Identify the blood parasite species.
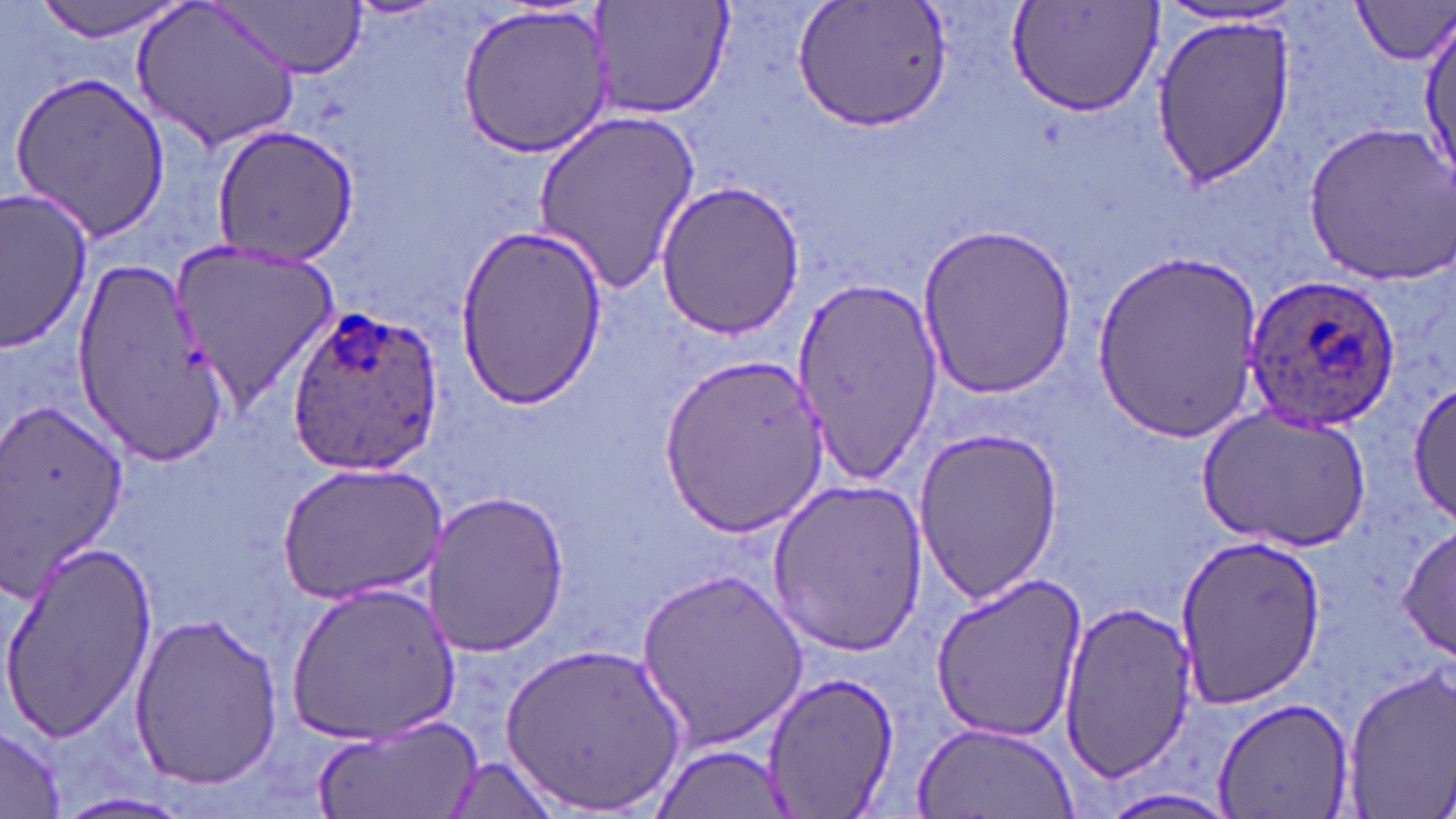

Plasmodium ovale.

Summary:
  - Coordinate format: approximate bounding boxes as [x1, y1, x2, y2] in pixels
  - Uninfected red blood cell locations: [31, 0, 192, 43], [131, 0, 305, 153], [597, 0, 735, 122], [792, 0, 953, 130], [1008, 0, 1165, 120], [1353, 2, 1455, 66], [213, 3, 364, 79], [456, 4, 615, 157], [1149, 4, 1303, 31], [1152, 14, 1295, 188], [1416, 17, 1453, 181], [6, 69, 170, 243], [532, 109, 702, 297], [1300, 117, 1455, 286], [208, 125, 358, 268], [655, 181, 808, 340], [0, 187, 94, 352], [916, 222, 1076, 400], [454, 225, 608, 410], [167, 240, 337, 411], [1092, 250, 1261, 441], [71, 256, 228, 458], [788, 276, 944, 485], [658, 355, 826, 537], [1408, 377, 1456, 526], [0, 393, 131, 609], [1198, 406, 1371, 553], [913, 426, 1065, 600], [275, 461, 446, 605], [766, 477, 928, 658], [421, 490, 571, 658], [1396, 525, 1456, 661], [1171, 536, 1326, 709], [1, 540, 157, 746], [634, 569, 813, 748], [927, 572, 1087, 745], [286, 581, 461, 742], [1056, 603, 1198, 779], [127, 608, 285, 790], [500, 640, 688, 814], [1339, 669, 1456, 811], [762, 671, 900, 818], [1211, 696, 1354, 819], [307, 714, 479, 819], [911, 719, 1080, 819], [0, 725, 69, 817], [651, 744, 796, 818], [439, 754, 562, 817], [56, 791, 195, 819], [1092, 791, 1241, 819]
  - Plasmodium ovale-infected red blood cell locations: [1234, 271, 1398, 432], [279, 304, 448, 483]
  - Stain: May-Grünwald-Giemsa
  - Modality: light microscopy
  - Image size: 1456×819 pixels
  - Field of view: single
  - Magnification: 1000x
  - Preparation: thin blood film